Report the malaria status of this cell.
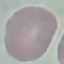

Uninfected.

{
  "capture": "smartphone through the microscope eyepiece",
  "preparation": "thin blood smear",
  "stain": "Giemsa",
  "image_type": "cell patch, automatically extracted from a larger field of view and resized to 64 × 64 pixels"
}